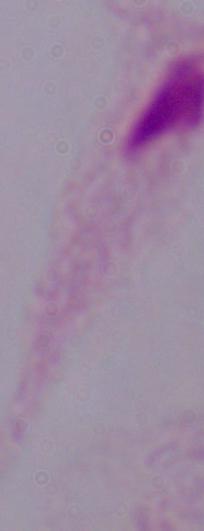

Photomicrograph. A trichomonad is seen. Captured at 1000x magnification.